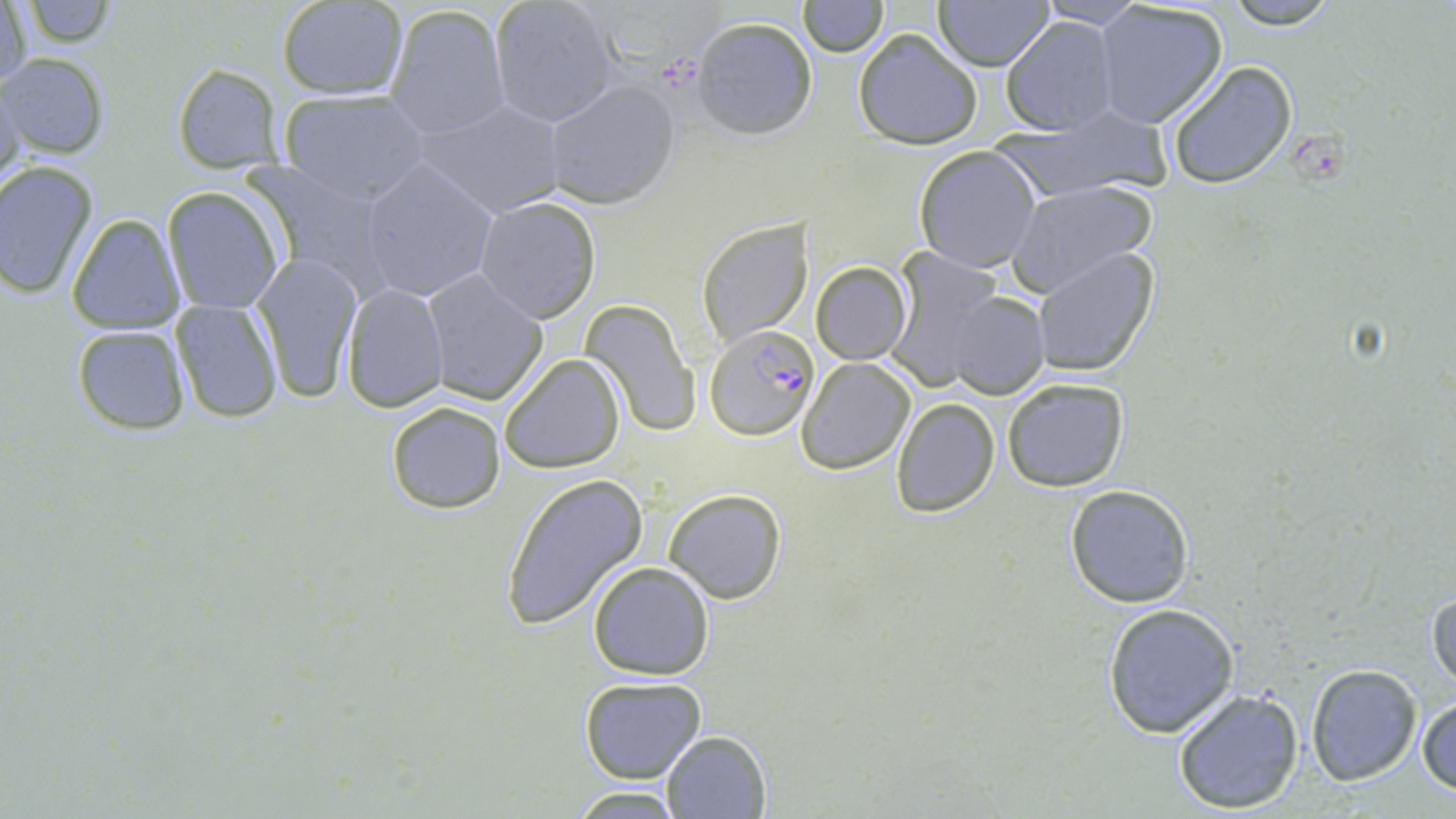 Approximate bounding boxes as (x1,y1)-(x2,y2) corner pairs in pixels. Uninfected red blood cell locations: (488,0)-(620,127), (934,0)-(1054,70), (1222,0)-(1345,29), (798,1)-(885,56), (1032,1)-(1147,27), (1,2)-(32,96), (19,2)-(121,48), (277,2)-(408,99), (1092,3)-(1229,129), (384,5)-(510,139), (691,15)-(819,141), (1000,16)-(1119,137), (853,29)-(984,149), (1,52)-(110,161), (1166,61)-(1298,190), (171,63)-(285,173), (0,79)-(27,196), (543,80)-(678,208), (278,89)-(431,202), (415,99)-(568,218), (991,110)-(1172,203), (913,147)-(1041,274), (0,159)-(99,299), (359,159)-(500,304), (240,161)-(396,291), (1006,181)-(1155,293), (161,185)-(285,314), (473,197)-(602,324), (66,212)-(185,335), (696,218)-(813,347), (1030,247)-(1159,378), (250,254)-(365,405), (890,257)-(1032,394), (810,262)-(911,365), (420,268)-(548,405), (340,283)-(449,413), (940,289)-(1050,399), (169,299)-(283,422), (580,299)-(700,439), (71,325)-(190,435), (501,354)-(626,474), (799,358)-(915,474), (1002,377)-(1130,492), (891,397)-(999,517), (384,400)-(507,515), (500,474)-(648,628), (1064,485)-(1195,608), (663,489)-(785,605), (586,562)-(715,681), (1427,583)-(1456,696), (1101,602)-(1242,738), (1304,665)-(1423,786), (578,676)-(707,784), (1171,684)-(1304,814), (1417,696)-(1456,798), (661,730)-(770,817), (569,787)-(689,817). Platelet locations: (1292,137)-(1346,183). Plasmodium falciparum-infected red blood cell locations: (706,325)-(817,441). Slide-level diagnosis: Plasmodium falciparum. Image is 1456×819 pixels. One field of a larger specimen. Light microscopy. Captured at 1000x magnification. Thin blood film. May-Grünwald-Giemsa stain.